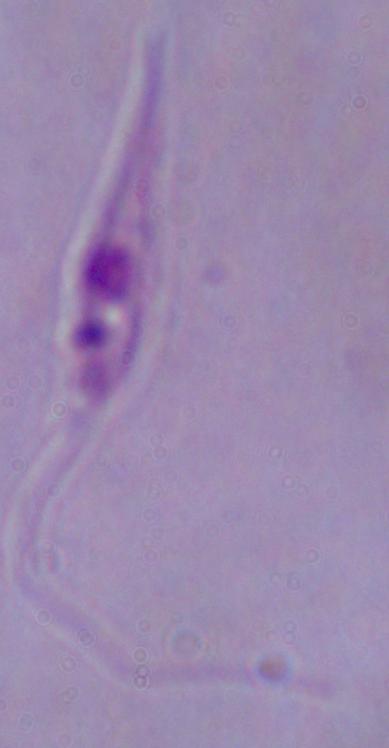

identification = Leishmania
magnification = 1000x
modality = photomicrograph